Assess the morphology of the erythrocytes.
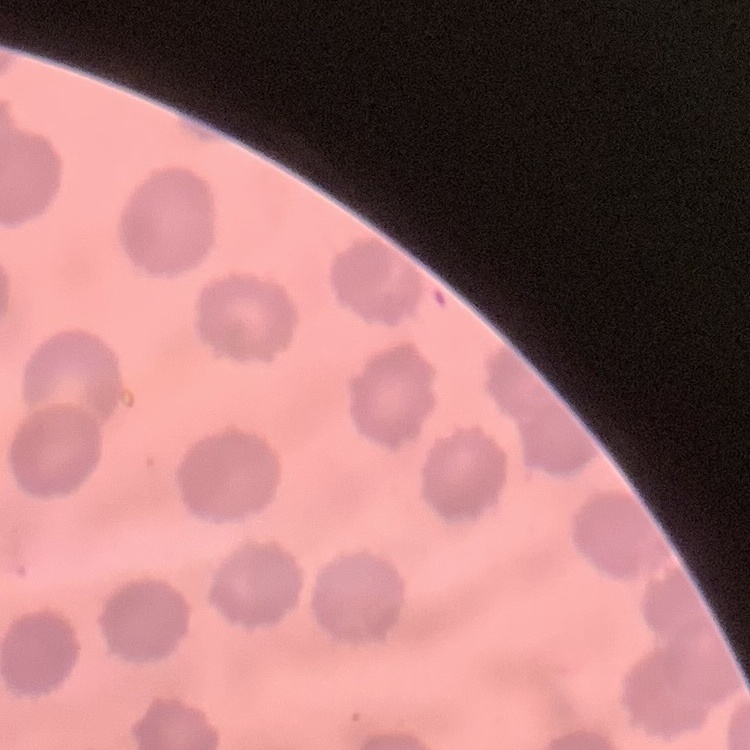

They show no rouleaux formation.

One tile cut from a larger photomicrograph. Stained with either Field's or Giemsa. Thin blood film.